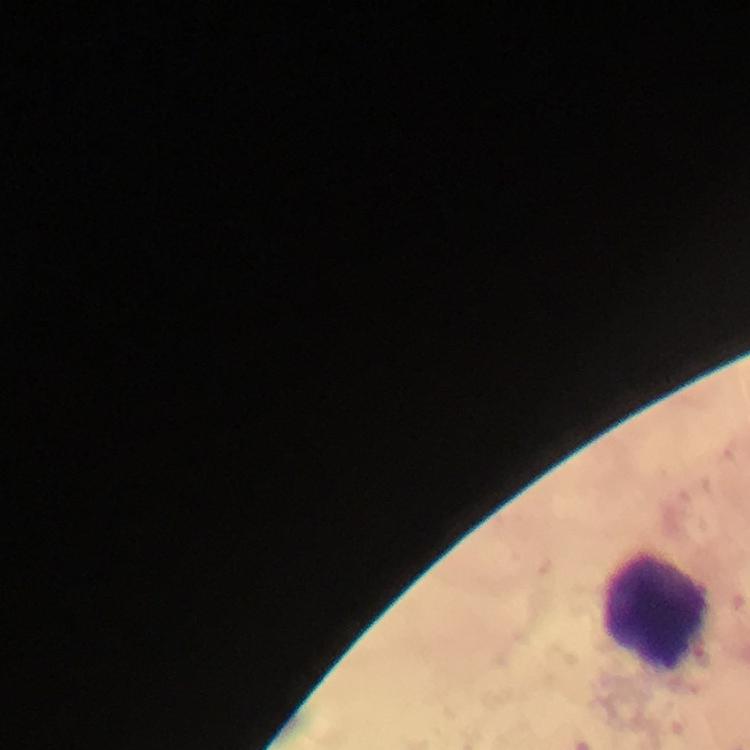

context = from a malaria diagnostic workup
magnification = 100x
preparation = thick smear
malaria parasites = none seen
cropped from = one field of view
capture = smartphone camera through the microscope
immersion oil = applied
stain = Giemsa
image size = 750×750 pixels
leukocyte locations = approximate centers as [x, y] in pixels: [658, 612]